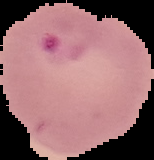
Malaria status: parasitized. Image is 154×160 pixels. From a thin blood film. Cell region segmented out of the field of view; the surrounding area is masked to black.